Classify this cell by malaria status.
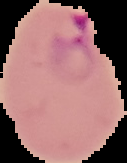

It is parasitized.

preparation: thin blood film
image_size: 127×163 pixels
image_type: cell region segmented out of the field of view; surrounding area masked to black